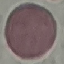
Summary:
  - Result: no malaria parasites detected
  - Capture: smartphone camera at the microscope eyepiece
  - Preparation: thin smear
  - Stain: Giemsa
  - Image type: cell patch, automatically extracted from a larger field of view and resized to 64 × 64 pixels